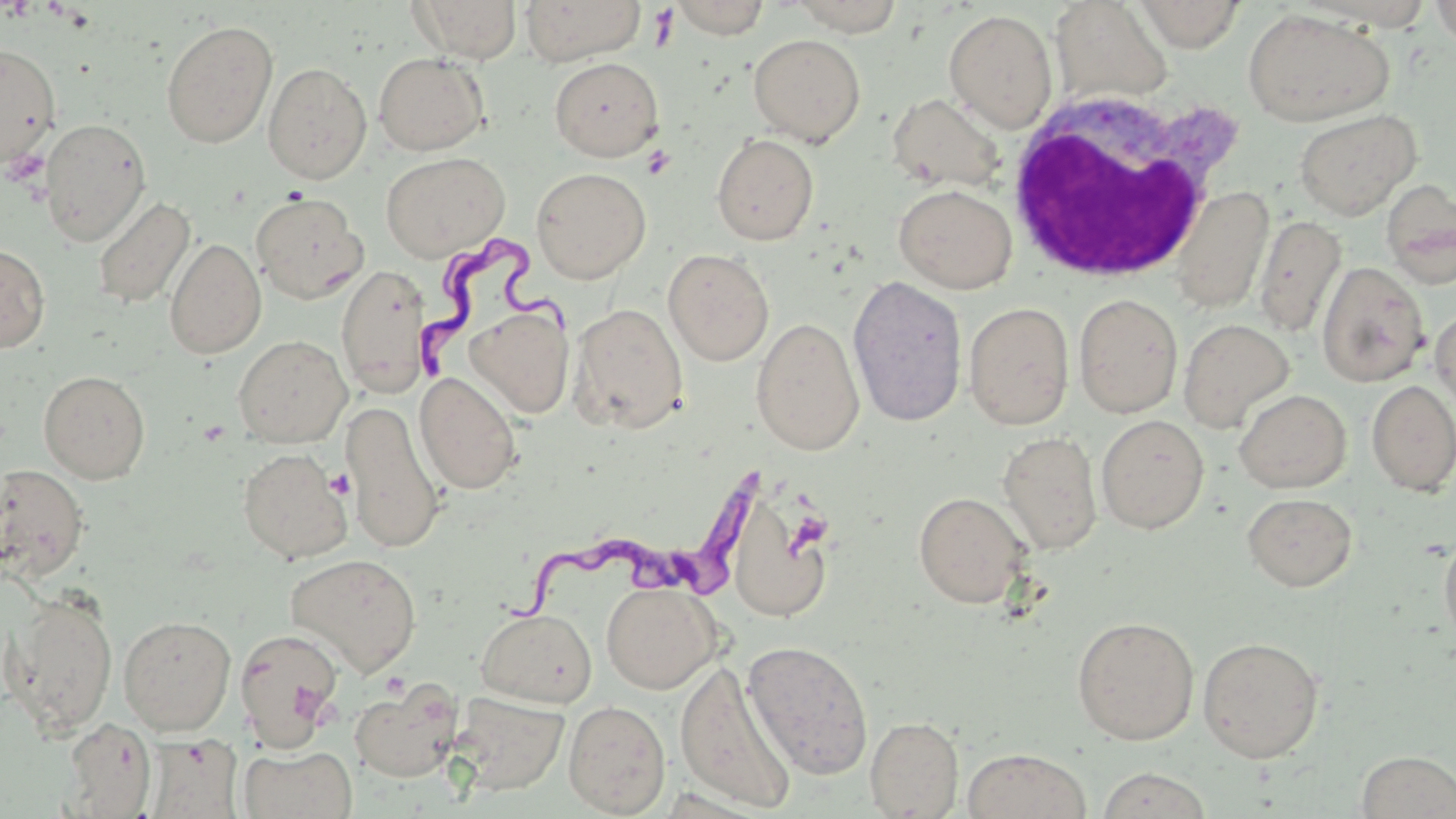
slide-level diagnosis = Trypanosoma brucei
field of view = single
platelet locations = approximate bounding boxes as (x1,y1)-(x2,y2) corner pairs in pixels: (641,145)-(677,180), (3,148)-(49,186), (325,470)-(354,500)
preparation = thin blood smear
uninfected red blood cell locations = approximate bounding boxes as (x1,y1)-(x2,y2) corner pairs in pixels: (409,0)-(522,63), (520,0)-(647,65), (671,0)-(770,39), (788,0)-(905,36), (1134,0)-(1245,52), (1429,0)-(1456,50), (1049,1)-(1173,105), (1242,8)-(1395,127), (944,9)-(1058,132), (161,20)-(278,147), (748,33)-(866,147), (0,42)-(62,166), (373,52)-(489,155), (550,57)-(664,161), (263,62)-(372,184), (887,93)-(1007,194), (1294,109)-(1421,220), (40,117)-(151,247), (711,133)-(819,245), (381,151)-(509,262), (531,167)-(651,283), (1381,180)-(1456,288), (894,183)-(1017,294), (1170,186)-(1274,313), (251,192)-(367,304), (92,196)-(196,309), (1254,214)-(1347,337), (165,237)-(266,359), (0,243)-(50,352), (663,248)-(774,365), (1316,261)-(1430,388), (335,263)-(432,398), (847,274)-(968,428), (1074,293)-(1183,418), (963,301)-(1074,430), (568,303)-(689,434), (1430,305)-(1456,411), (466,306)-(574,418), (751,317)-(865,454), (1179,318)-(1295,431), (233,335)-(352,447), (38,370)-(151,483), (415,372)-(522,494), (1366,380)-(1456,496), (1234,389)-(1351,493), (340,400)-(445,556), (1096,414)-(1209,534), (998,431)-(1103,555), (237,447)-(352,563), (0,464)-(90,583), (913,491)-(1032,608), (1243,492)-(1357,591), (733,503)-(831,620), (1439,527)-(1456,654), (284,552)-(422,677), (601,581)-(721,693), (3,590)-(118,737), (476,607)-(597,707), (117,615)-(237,735), (1071,616)-(1199,745), (234,627)-(344,751), (1198,636)-(1325,763), (742,639)-(875,779), (674,661)-(798,812), (349,678)-(462,783), (449,692)-(569,795), (563,699)-(671,817), (865,716)-(964,818), (60,717)-(158,818), (143,734)-(241,818), (238,745)-(357,819), (962,747)-(1093,819), (1355,750)-(1456,818), (1094,767)-(1216,819)
modality = optical microscopy
magnification = 1000x
stain = May-Grünwald-Giemsa
Trypanosoma brucei locations = approximate bounding boxes as (x1,y1)-(x2,y2) corner pairs in pixels: (414,238)-(580,391), (503,463)-(776,628)
image size = 1456×819 pixels
white blood cell locations = approximate bounding boxes as (x1,y1)-(x2,y2) corner pairs in pixels: (998,90)-(1238,287)